Evaluate for Plasmodium parasites.
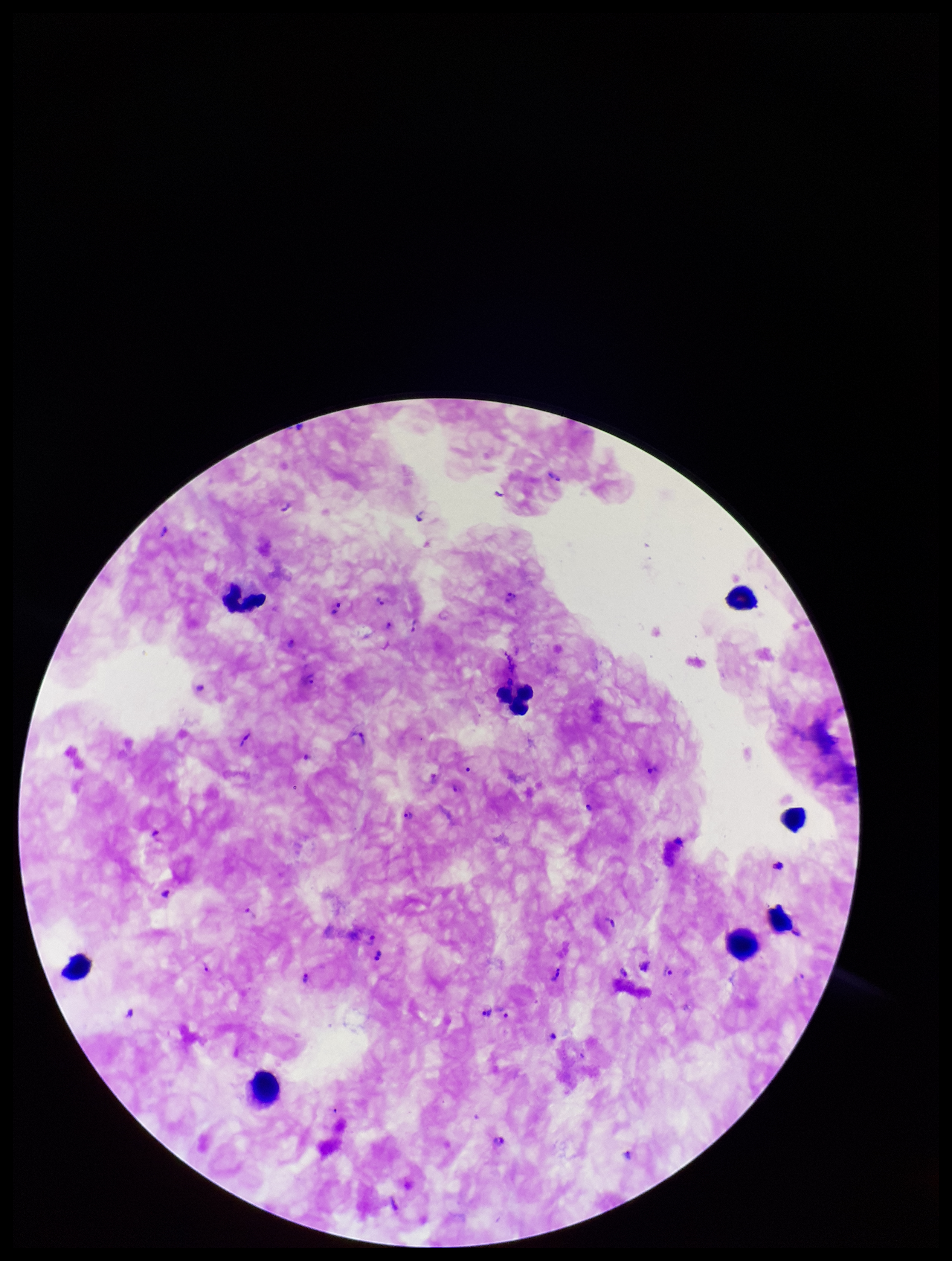
Detected.

Parasite count: 24. Preparation: thick smear. Giemsa stain. Patient malaria status: infected. One field from this slide. Leukocyte count: 8. Species reported for this patient: Plasmodium falciparum. Photographed through the microscope eyepiece with a smartphone camera. Image is 952×1261 pixels.